Identify the cell.
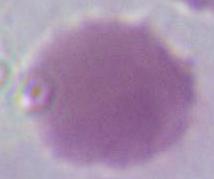

An erythrocyte.

magnification: 1000x
modality: micrograph